Name the parasite shown.
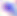
This is Toxoplasma gondii.

magnification = 400x
modality = photomicrograph